State which parasite is depicted.
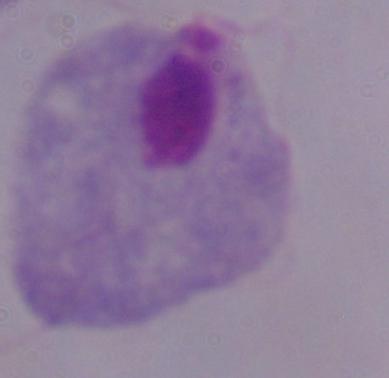
A trichomonad.

1000x magnification. Micrograph.